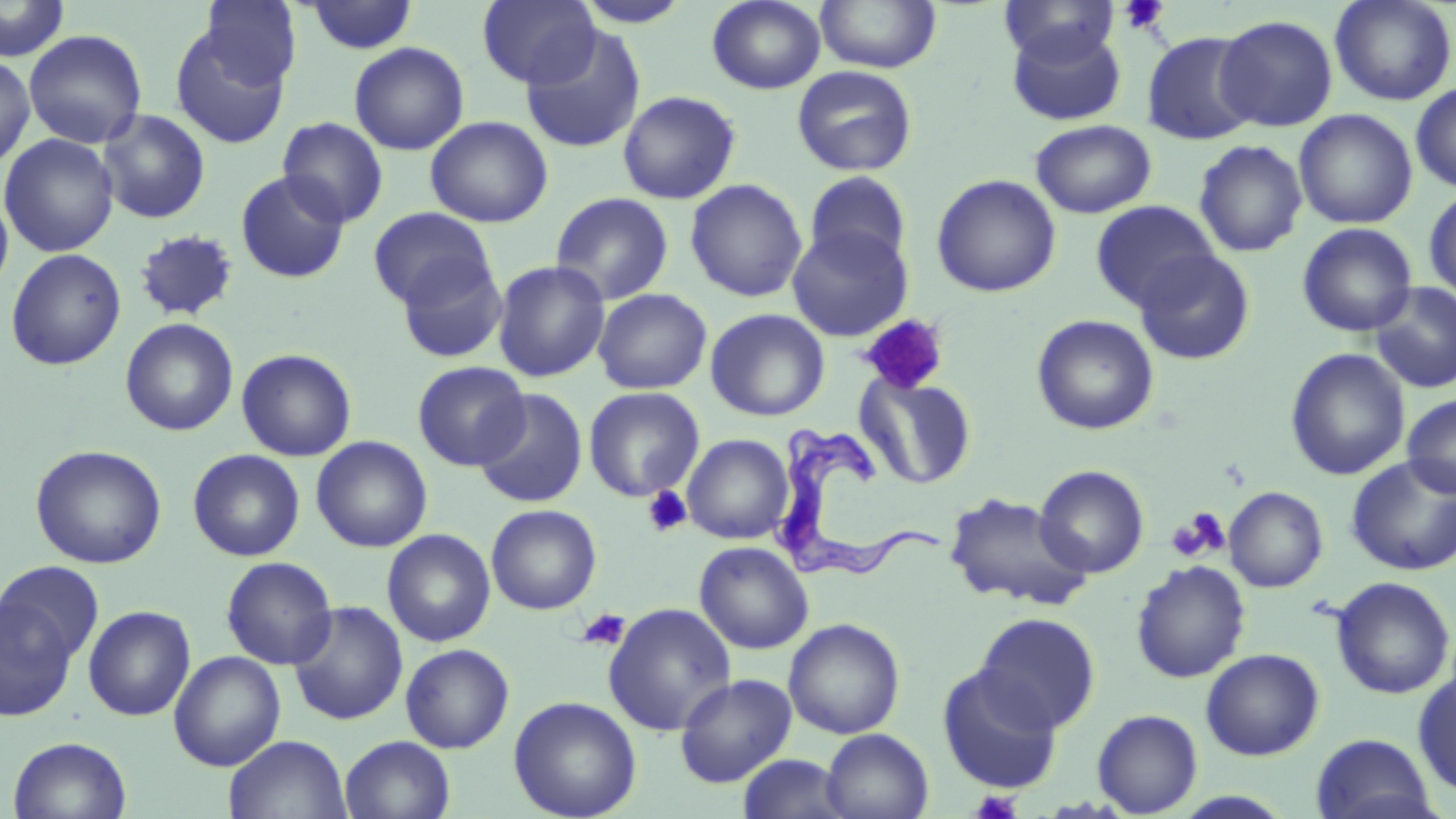

{
  "slide_level_diagnosis": "Trypanosoma brucei",
  "stain": "May-Grünwald-Giemsa",
  "magnification": "1000x",
  "platelet_locations": "approximate bounding boxes as [x1, y1, x2, y2] in pixels: [1118, 0, 1171, 35], [858, 314, 950, 394], [642, 486, 692, 537], [1169, 509, 1228, 560], [576, 607, 631, 651], [971, 789, 1023, 819]",
  "trypanosoma_brucei_locations": "approximate bounding boxes as [x1, y1, x2, y2] in pixels: [771, 420, 948, 589]",
  "field_of_view": "single",
  "image_size": "1456×819 pixels",
  "uninfected_red_blood_cell_locations": "approximate bounding boxes as [x1, y1, x2, y2] in pixels: [0, 0, 70, 61], [199, 0, 301, 90], [303, 0, 420, 55], [476, 0, 601, 88], [706, 0, 827, 94], [815, 0, 942, 73], [999, 0, 1121, 64], [1329, 0, 1456, 106], [571, 3, 694, 29], [1215, 14, 1338, 132], [1007, 23, 1127, 127], [519, 25, 647, 154], [170, 27, 290, 149], [24, 29, 147, 148], [1141, 31, 1261, 145], [348, 42, 469, 155], [0, 58, 36, 169], [792, 65, 918, 177], [1410, 82, 1456, 193], [617, 90, 741, 205], [96, 109, 211, 224], [1294, 109, 1418, 229], [425, 115, 553, 228], [276, 117, 389, 228], [1030, 119, 1156, 219], [0, 134, 120, 257], [1193, 140, 1308, 257], [235, 169, 350, 283], [803, 171, 913, 272], [930, 174, 1061, 298], [685, 178, 807, 302], [1423, 187, 1456, 302], [0, 191, 14, 299], [549, 192, 674, 306], [1090, 200, 1219, 311], [367, 207, 496, 309], [523, 211, 649, 342], [1297, 222, 1418, 337], [786, 225, 913, 341], [133, 229, 239, 322], [5, 248, 126, 370], [1134, 249, 1256, 365], [394, 255, 508, 364], [491, 260, 610, 383], [1369, 282, 1456, 394], [593, 288, 712, 395], [705, 308, 830, 421], [1031, 315, 1159, 435], [120, 317, 239, 436], [236, 348, 357, 462], [1285, 348, 1410, 481], [412, 360, 530, 471], [855, 373, 977, 489], [583, 387, 704, 502], [473, 388, 589, 509], [1402, 394, 1456, 498], [682, 434, 794, 544], [311, 435, 432, 553], [30, 444, 167, 569], [187, 449, 305, 561], [1346, 455, 1456, 576], [1034, 465, 1149, 578], [1224, 486, 1328, 592], [944, 491, 1091, 611], [486, 504, 602, 614], [381, 528, 496, 647], [694, 541, 814, 654], [220, 555, 338, 670], [0, 560, 105, 666], [1131, 560, 1251, 683], [1330, 576, 1455, 700], [0, 595, 78, 722], [287, 600, 408, 726], [602, 602, 737, 736], [83, 605, 196, 721], [974, 612, 1100, 733], [783, 618, 906, 739], [400, 643, 515, 753], [1200, 648, 1325, 761], [168, 651, 286, 771], [937, 666, 1063, 794], [1413, 668, 1456, 798], [674, 673, 797, 787], [508, 695, 642, 819], [1091, 708, 1203, 817], [821, 728, 934, 819], [1310, 733, 1438, 819], [223, 734, 353, 819], [6, 735, 132, 819], [339, 735, 456, 819], [737, 754, 851, 818], [1170, 790, 1296, 818]",
  "preparation": "thin blood film",
  "modality": "optical microscopy"
}